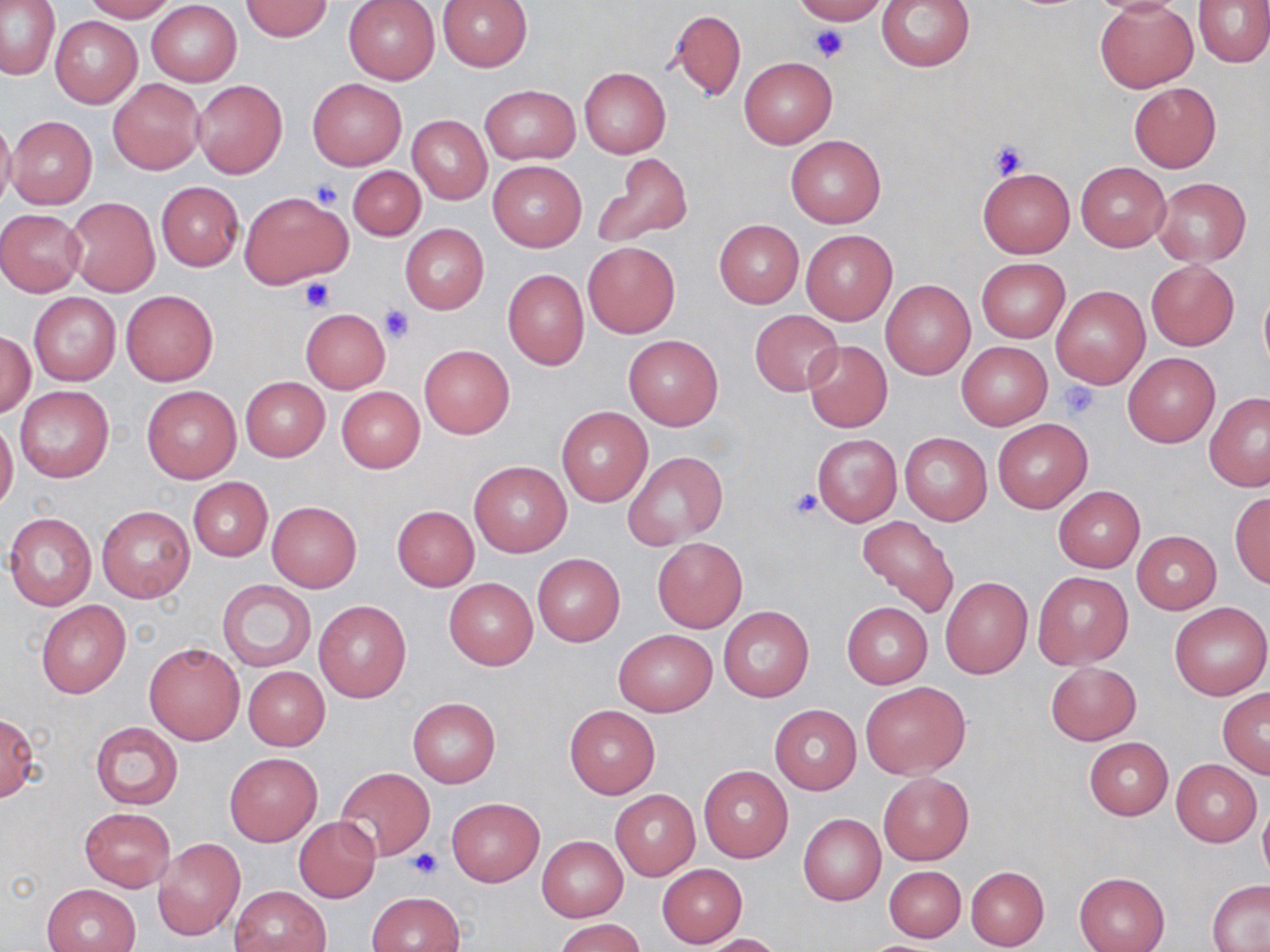 Approximate bounding boxes as named x1/y1/x2/y2 corners in pixels. Uninfected red blood cell locations: (x1=1, y1=0, x2=61, y2=80), (x1=83, y1=0, x2=176, y2=22), (x1=793, y1=0, x2=888, y2=25), (x1=877, y1=0, x2=975, y2=72), (x1=1086, y1=0, x2=1187, y2=16), (x1=1194, y1=0, x2=1270, y2=67), (x1=148, y1=1, x2=242, y2=86), (x1=241, y1=1, x2=334, y2=41), (x1=344, y1=1, x2=440, y2=85), (x1=436, y1=1, x2=533, y2=70), (x1=1095, y1=2, x2=1198, y2=92), (x1=667, y1=8, x2=746, y2=103), (x1=51, y1=16, x2=142, y2=107), (x1=738, y1=55, x2=837, y2=149), (x1=579, y1=67, x2=670, y2=160), (x1=306, y1=79, x2=407, y2=170), (x1=109, y1=80, x2=204, y2=174), (x1=192, y1=80, x2=287, y2=177), (x1=1130, y1=82, x2=1221, y2=172), (x1=480, y1=85, x2=579, y2=164), (x1=0, y1=112, x2=16, y2=215), (x1=7, y1=115, x2=96, y2=210), (x1=408, y1=116, x2=491, y2=205), (x1=785, y1=134, x2=885, y2=227), (x1=592, y1=154, x2=693, y2=249), (x1=489, y1=161, x2=586, y2=251), (x1=1076, y1=162, x2=1171, y2=251), (x1=348, y1=166, x2=426, y2=241), (x1=977, y1=166, x2=1074, y2=257), (x1=1152, y1=177, x2=1251, y2=265), (x1=156, y1=182, x2=243, y2=270), (x1=238, y1=192, x2=349, y2=288), (x1=64, y1=198, x2=160, y2=297), (x1=0, y1=210, x2=85, y2=295), (x1=714, y1=219, x2=803, y2=308), (x1=400, y1=225, x2=488, y2=313), (x1=801, y1=229, x2=897, y2=325), (x1=583, y1=243, x2=680, y2=338), (x1=975, y1=258, x2=1070, y2=343), (x1=1146, y1=260, x2=1239, y2=350), (x1=503, y1=268, x2=589, y2=369), (x1=881, y1=280, x2=975, y2=379), (x1=1052, y1=285, x2=1150, y2=389), (x1=1258, y1=285, x2=1270, y2=380), (x1=121, y1=290, x2=218, y2=385), (x1=28, y1=292, x2=121, y2=385), (x1=300, y1=309, x2=390, y2=393), (x1=750, y1=311, x2=842, y2=395), (x1=1, y1=331, x2=36, y2=418), (x1=623, y1=334, x2=722, y2=430), (x1=802, y1=340, x2=892, y2=433), (x1=957, y1=342, x2=1052, y2=429), (x1=418, y1=345, x2=514, y2=438), (x1=1123, y1=353, x2=1219, y2=447), (x1=241, y1=377, x2=330, y2=461), (x1=142, y1=385, x2=241, y2=483), (x1=15, y1=386, x2=113, y2=483), (x1=337, y1=387, x2=424, y2=472), (x1=1205, y1=392, x2=1270, y2=491), (x1=556, y1=407, x2=653, y2=506), (x1=992, y1=418, x2=1092, y2=513), (x1=0, y1=419, x2=18, y2=511), (x1=811, y1=432, x2=901, y2=527), (x1=900, y1=432, x2=992, y2=526), (x1=623, y1=451, x2=727, y2=548), (x1=469, y1=461, x2=571, y2=556), (x1=187, y1=477, x2=273, y2=562), (x1=1053, y1=486, x2=1144, y2=572), (x1=1229, y1=492, x2=1270, y2=589), (x1=267, y1=501, x2=362, y2=592), (x1=97, y1=505, x2=194, y2=603), (x1=391, y1=505, x2=479, y2=591), (x1=3, y1=512, x2=97, y2=610), (x1=857, y1=515, x2=960, y2=619), (x1=1132, y1=530, x2=1220, y2=614), (x1=652, y1=537, x2=747, y2=633), (x1=533, y1=554, x2=624, y2=645), (x1=1033, y1=572, x2=1132, y2=668), (x1=940, y1=576, x2=1033, y2=679), (x1=444, y1=577, x2=538, y2=670), (x1=216, y1=580, x2=315, y2=672), (x1=36, y1=601, x2=130, y2=698), (x1=1169, y1=601, x2=1270, y2=700), (x1=315, y1=602, x2=410, y2=702), (x1=842, y1=602, x2=932, y2=689), (x1=718, y1=606, x2=813, y2=702), (x1=614, y1=629, x2=716, y2=716), (x1=143, y1=642, x2=246, y2=745), (x1=1046, y1=662, x2=1140, y2=744), (x1=243, y1=666, x2=329, y2=750), (x1=859, y1=681, x2=971, y2=779), (x1=1217, y1=688, x2=1270, y2=777), (x1=408, y1=698, x2=501, y2=788), (x1=563, y1=704, x2=661, y2=798), (x1=769, y1=704, x2=862, y2=795), (x1=0, y1=713, x2=41, y2=802), (x1=90, y1=722, x2=183, y2=809), (x1=1083, y1=737, x2=1173, y2=820), (x1=225, y1=751, x2=321, y2=846), (x1=1172, y1=759, x2=1262, y2=846), (x1=698, y1=765, x2=794, y2=862), (x1=336, y1=768, x2=435, y2=861), (x1=877, y1=772, x2=974, y2=865), (x1=609, y1=789, x2=700, y2=881), (x1=446, y1=797, x2=544, y2=886), (x1=1258, y1=799, x2=1270, y2=884), (x1=79, y1=807, x2=176, y2=892), (x1=798, y1=814, x2=885, y2=904), (x1=293, y1=816, x2=381, y2=901), (x1=537, y1=836, x2=627, y2=921), (x1=152, y1=837, x2=246, y2=942), (x1=656, y1=864, x2=747, y2=947), (x1=884, y1=866, x2=966, y2=942), (x1=965, y1=866, x2=1049, y2=950), (x1=1074, y1=872, x2=1169, y2=952), (x1=1207, y1=881, x2=1270, y2=951), (x1=42, y1=883, x2=141, y2=952), (x1=230, y1=885, x2=331, y2=952), (x1=367, y1=892, x2=465, y2=951), (x1=556, y1=918, x2=646, y2=952), (x1=698, y1=933, x2=783, y2=952). Platelet locations: (x1=810, y1=25, x2=847, y2=64), (x1=988, y1=139, x2=1029, y2=180), (x1=312, y1=178, x2=343, y2=209), (x1=299, y1=278, x2=333, y2=311), (x1=380, y1=303, x2=415, y2=344), (x1=1057, y1=381, x2=1102, y2=422), (x1=789, y1=488, x2=824, y2=520), (x1=407, y1=846, x2=444, y2=879). Slide-level diagnosis: negative for blood parasites. Captured at 1000x magnification. Optical microscopy. May-Grünwald-Giemsa stain. Image is 1270×952 pixels. Thin blood film. Single field of view.